Assess this cell for malaria.
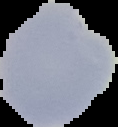
Parasitized.

Summary:
  - Image size: 118×127 pixels
  - Image type: cell region segmented out of the field of view; surrounding area masked to black
  - Preparation: thin blood film